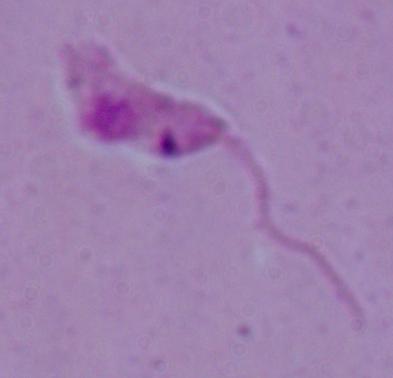

A Leishmania parasite is seen. Captured at 1000x magnification. Micrograph.